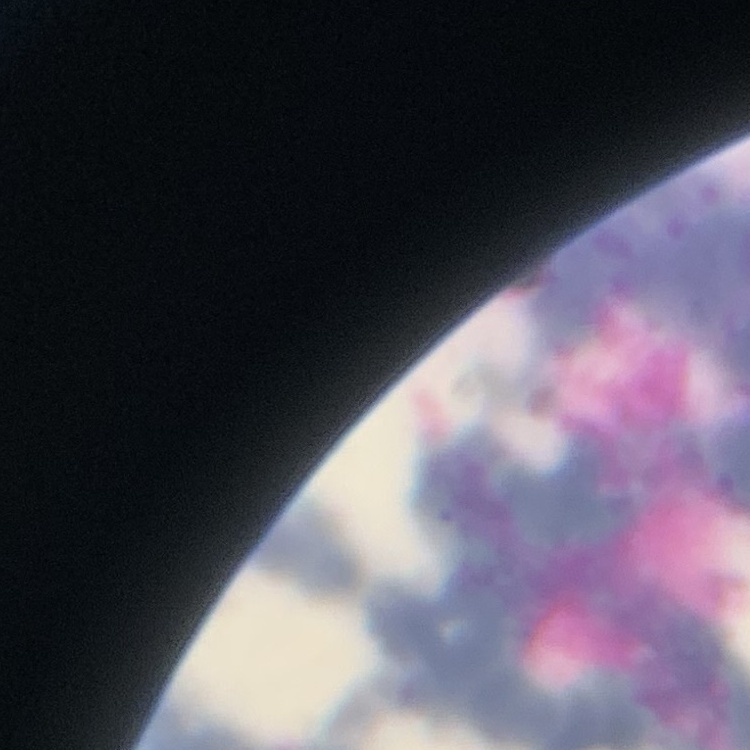

Summary:
  - Red blood cell morphology: rouleaux formation
  - Preparation: thin blood smear
  - Image type: one tile cut from a larger photomicrograph
  - Stain: Field's or Giemsa